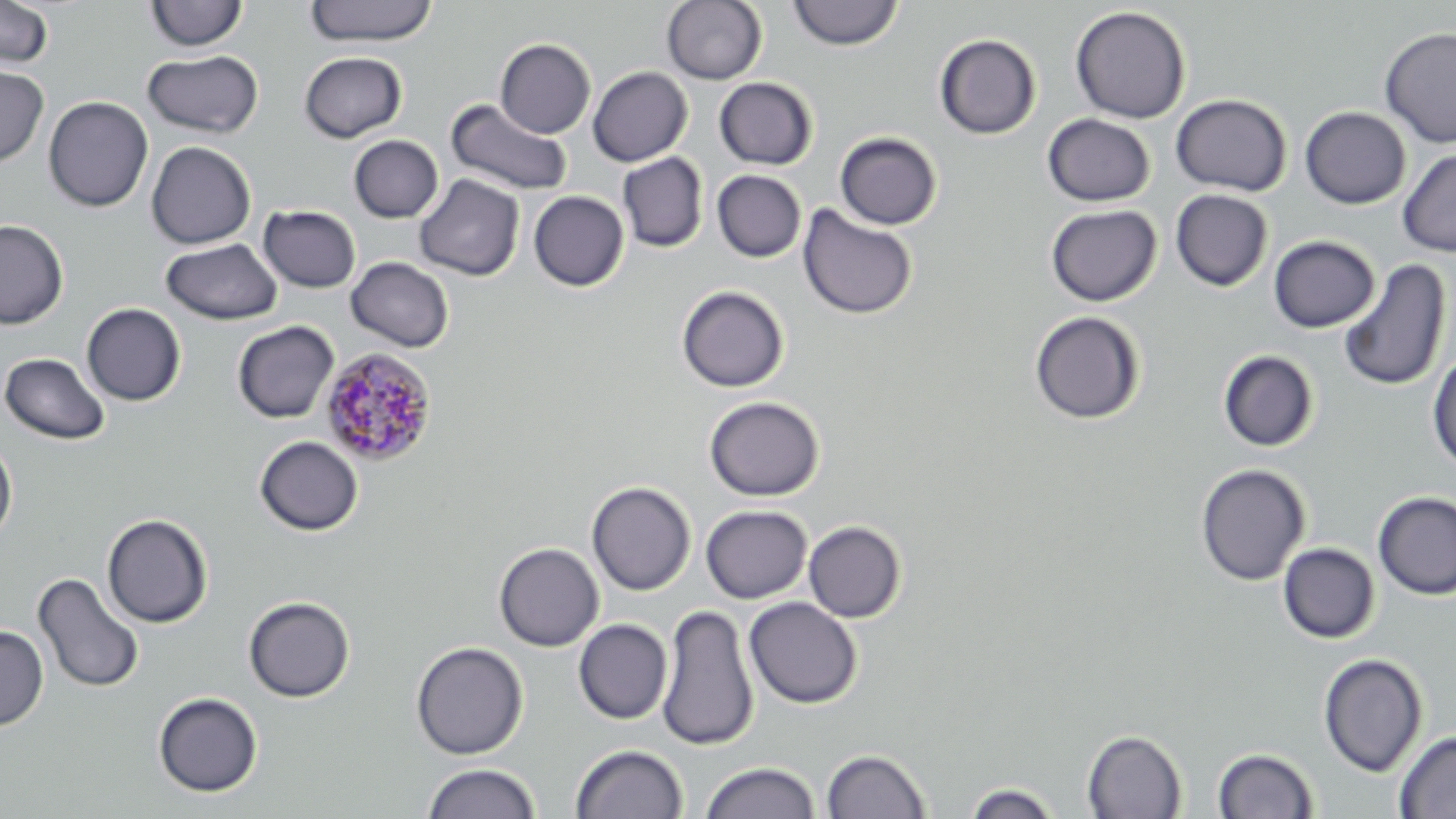

Summary:
  - Coordinate format: approximate bounding boxes as named x1/y1/x2/y2 corners in pixels
  - Uninfected red blood cell locations: (x1=0, y1=0, x2=55, y2=70), (x1=305, y1=0, x2=438, y2=47), (x1=661, y1=0, x2=767, y2=85), (x1=144, y1=1, x2=248, y2=53), (x1=787, y1=1, x2=904, y2=51), (x1=1069, y1=5, x2=1191, y2=123), (x1=1378, y1=26, x2=1456, y2=149), (x1=934, y1=34, x2=1041, y2=140), (x1=495, y1=38, x2=595, y2=138), (x1=143, y1=50, x2=264, y2=139), (x1=299, y1=51, x2=408, y2=142), (x1=0, y1=63, x2=49, y2=168), (x1=588, y1=66, x2=692, y2=166), (x1=714, y1=77, x2=818, y2=170), (x1=1171, y1=94, x2=1292, y2=196), (x1=43, y1=96, x2=153, y2=212), (x1=445, y1=98, x2=573, y2=197), (x1=1300, y1=106, x2=1411, y2=209), (x1=1042, y1=114, x2=1156, y2=206), (x1=834, y1=131, x2=943, y2=230), (x1=349, y1=135, x2=443, y2=222), (x1=146, y1=141, x2=256, y2=249), (x1=1397, y1=148, x2=1456, y2=257), (x1=617, y1=152, x2=708, y2=252), (x1=711, y1=170, x2=806, y2=262), (x1=414, y1=174, x2=525, y2=281), (x1=1170, y1=189, x2=1274, y2=291), (x1=528, y1=191, x2=629, y2=291), (x1=797, y1=203, x2=918, y2=320), (x1=1045, y1=204, x2=1162, y2=306), (x1=258, y1=205, x2=361, y2=293), (x1=0, y1=219, x2=68, y2=329), (x1=1268, y1=235, x2=1379, y2=333), (x1=161, y1=237, x2=283, y2=325), (x1=345, y1=257, x2=454, y2=353), (x1=1337, y1=258, x2=1451, y2=393), (x1=676, y1=285, x2=789, y2=393), (x1=82, y1=303, x2=186, y2=406), (x1=1028, y1=311, x2=1146, y2=425), (x1=232, y1=321, x2=339, y2=423), (x1=1218, y1=350, x2=1319, y2=451), (x1=1427, y1=350, x2=1456, y2=472), (x1=1, y1=351, x2=111, y2=446), (x1=703, y1=396, x2=825, y2=501), (x1=254, y1=436, x2=363, y2=535), (x1=0, y1=439, x2=17, y2=544), (x1=1194, y1=463, x2=1311, y2=586), (x1=586, y1=481, x2=696, y2=595), (x1=1372, y1=491, x2=1456, y2=600), (x1=701, y1=505, x2=812, y2=603), (x1=102, y1=513, x2=213, y2=628), (x1=804, y1=520, x2=906, y2=622), (x1=494, y1=542, x2=604, y2=651), (x1=1278, y1=542, x2=1380, y2=643), (x1=32, y1=572, x2=145, y2=694), (x1=243, y1=596, x2=355, y2=703), (x1=744, y1=597, x2=862, y2=709), (x1=656, y1=603, x2=759, y2=751), (x1=574, y1=619, x2=672, y2=724), (x1=0, y1=625, x2=49, y2=730), (x1=410, y1=641, x2=528, y2=759), (x1=1318, y1=653, x2=1427, y2=776), (x1=153, y1=692, x2=263, y2=797), (x1=1081, y1=729, x2=1187, y2=818), (x1=1393, y1=729, x2=1456, y2=818), (x1=570, y1=744, x2=688, y2=819), (x1=1212, y1=747, x2=1319, y2=818), (x1=821, y1=748, x2=932, y2=819), (x1=700, y1=761, x2=820, y2=819), (x1=421, y1=762, x2=541, y2=819), (x1=964, y1=781, x2=1062, y2=818)
  - Plasmodium malariae-infected red blood cell locations: (x1=319, y1=347, x2=437, y2=467)
  - Slide-level diagnosis: Plasmodium malariae
  - Magnification: 1000x
  - Preparation: thin blood film
  - Image size: 1456×819 pixels
  - Stain: May-Grünwald-Giemsa
  - Modality: optical microscopy
  - Field of view: single